Outline each blood parasite and name the species.
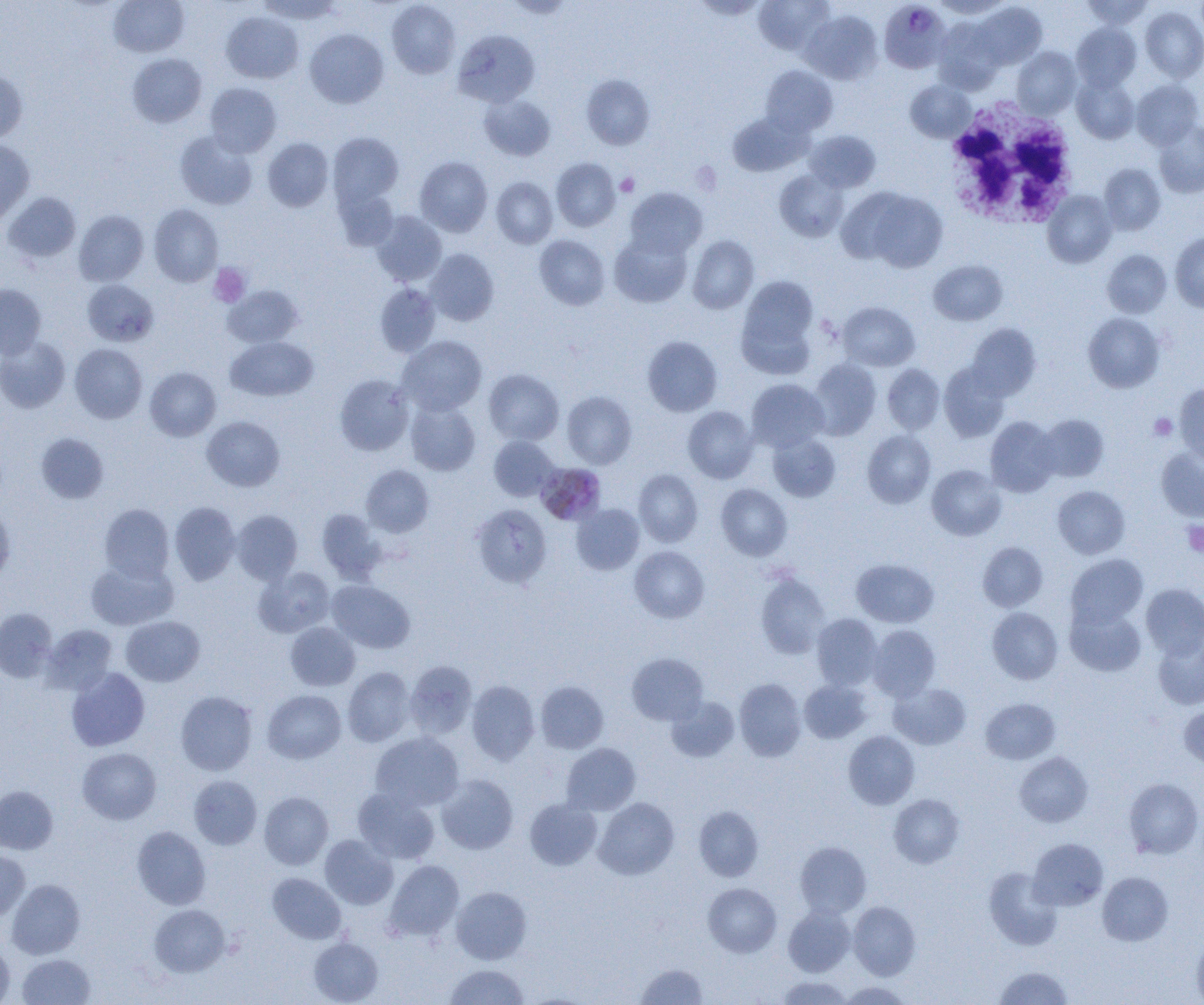

Approximate bounding boxes as named x1/y1/x2/y2 corners in pixels.
Plasmodium malariae-infected red blood cells: (x1=879, y1=1, x2=952, y2=74), (x1=538, y1=463, x2=608, y2=522).
No Plasmodium falciparum, Plasmodium ovale, Plasmodium vivax, Babesia divergens, or Trypanosoma brucei observed.

Platelet locations: (x1=616, y1=173, x2=639, y2=196), (x1=209, y1=263, x2=250, y2=307), (x1=1149, y1=414, x2=1177, y2=440), (x1=1182, y1=521, x2=1204, y2=557). White blood cell locations: (x1=941, y1=98, x2=1082, y2=229). Uninfected red blood cell locations: (x1=109, y1=0, x2=189, y2=57), (x1=257, y1=0, x2=344, y2=24), (x1=753, y1=0, x2=833, y2=55), (x1=930, y1=0, x2=1011, y2=19), (x1=1081, y1=0, x2=1154, y2=30), (x1=386, y1=1, x2=460, y2=78), (x1=972, y1=3, x2=1047, y2=69), (x1=1140, y1=5, x2=1204, y2=83), (x1=801, y1=10, x2=883, y2=85), (x1=221, y1=12, x2=303, y2=84), (x1=933, y1=19, x2=1005, y2=93), (x1=1071, y1=23, x2=1141, y2=92), (x1=305, y1=29, x2=389, y2=108), (x1=454, y1=29, x2=539, y2=107), (x1=1012, y1=47, x2=1081, y2=119), (x1=128, y1=53, x2=207, y2=127), (x1=760, y1=65, x2=837, y2=137), (x1=0, y1=68, x2=28, y2=143), (x1=581, y1=74, x2=655, y2=150), (x1=1072, y1=75, x2=1139, y2=144), (x1=1131, y1=79, x2=1203, y2=149), (x1=905, y1=80, x2=975, y2=142), (x1=205, y1=83, x2=281, y2=157), (x1=479, y1=93, x2=555, y2=161), (x1=728, y1=112, x2=810, y2=176), (x1=1154, y1=121, x2=1204, y2=198), (x1=804, y1=130, x2=880, y2=192), (x1=175, y1=131, x2=258, y2=209), (x1=328, y1=133, x2=403, y2=208), (x1=263, y1=137, x2=333, y2=212), (x1=0, y1=140, x2=34, y2=225), (x1=415, y1=156, x2=492, y2=237), (x1=551, y1=158, x2=620, y2=231), (x1=1099, y1=164, x2=1165, y2=235), (x1=774, y1=170, x2=848, y2=242), (x1=491, y1=177, x2=557, y2=248), (x1=334, y1=187, x2=399, y2=251), (x1=624, y1=187, x2=707, y2=258), (x1=851, y1=189, x2=948, y2=272), (x1=1043, y1=191, x2=1117, y2=268), (x1=3, y1=192, x2=81, y2=263), (x1=149, y1=204, x2=223, y2=286), (x1=74, y1=210, x2=149, y2=286), (x1=371, y1=211, x2=447, y2=287), (x1=609, y1=232, x2=692, y2=308), (x1=1170, y1=232, x2=1204, y2=313), (x1=534, y1=235, x2=610, y2=310), (x1=687, y1=235, x2=759, y2=314), (x1=425, y1=249, x2=499, y2=325), (x1=1102, y1=249, x2=1172, y2=318), (x1=928, y1=260, x2=1007, y2=325), (x1=738, y1=275, x2=819, y2=366), (x1=82, y1=279, x2=158, y2=347), (x1=375, y1=283, x2=440, y2=357), (x1=0, y1=284, x2=46, y2=359), (x1=223, y1=285, x2=303, y2=348), (x1=838, y1=302, x2=920, y2=371), (x1=1083, y1=312, x2=1165, y2=392), (x1=966, y1=323, x2=1041, y2=401), (x1=225, y1=336, x2=318, y2=401), (x1=397, y1=336, x2=487, y2=415), (x1=642, y1=336, x2=723, y2=416), (x1=0, y1=337, x2=70, y2=413), (x1=70, y1=344, x2=147, y2=423), (x1=808, y1=358, x2=882, y2=440), (x1=882, y1=363, x2=945, y2=434), (x1=939, y1=363, x2=1010, y2=442), (x1=145, y1=367, x2=221, y2=441), (x1=484, y1=368, x2=564, y2=445), (x1=334, y1=374, x2=414, y2=456), (x1=746, y1=379, x2=829, y2=452), (x1=1174, y1=383, x2=1204, y2=466), (x1=561, y1=391, x2=636, y2=469), (x1=406, y1=400, x2=481, y2=476), (x1=682, y1=406, x2=758, y2=483), (x1=1037, y1=414, x2=1109, y2=482), (x1=202, y1=416, x2=284, y2=491), (x1=985, y1=416, x2=1060, y2=497), (x1=862, y1=430, x2=936, y2=508), (x1=36, y1=433, x2=109, y2=504), (x1=768, y1=434, x2=840, y2=502), (x1=489, y1=435, x2=559, y2=501), (x1=1156, y1=448, x2=1204, y2=521), (x1=927, y1=464, x2=1006, y2=540), (x1=361, y1=465, x2=434, y2=537), (x1=634, y1=469, x2=703, y2=546), (x1=716, y1=484, x2=792, y2=560), (x1=1052, y1=485, x2=1130, y2=559), (x1=169, y1=502, x2=241, y2=585), (x1=100, y1=503, x2=175, y2=581), (x1=472, y1=503, x2=552, y2=588), (x1=572, y1=504, x2=644, y2=574), (x1=0, y1=505, x2=15, y2=583), (x1=316, y1=509, x2=386, y2=582), (x1=232, y1=510, x2=303, y2=584), (x1=978, y1=542, x2=1048, y2=611), (x1=629, y1=546, x2=709, y2=623), (x1=1065, y1=554, x2=1148, y2=630), (x1=851, y1=558, x2=938, y2=627), (x1=86, y1=559, x2=178, y2=630), (x1=254, y1=567, x2=335, y2=637), (x1=755, y1=571, x2=830, y2=659), (x1=327, y1=580, x2=415, y2=653), (x1=1141, y1=583, x2=1204, y2=659), (x1=1065, y1=605, x2=1146, y2=676), (x1=987, y1=607, x2=1063, y2=684), (x1=0, y1=608, x2=57, y2=683), (x1=811, y1=613, x2=882, y2=690), (x1=121, y1=616, x2=205, y2=686), (x1=285, y1=622, x2=360, y2=690), (x1=42, y1=624, x2=117, y2=694), (x1=867, y1=624, x2=940, y2=701), (x1=1153, y1=634, x2=1204, y2=709), (x1=627, y1=652, x2=708, y2=725), (x1=405, y1=660, x2=477, y2=738), (x1=66, y1=667, x2=150, y2=751), (x1=342, y1=667, x2=415, y2=746), (x1=734, y1=678, x2=806, y2=761), (x1=466, y1=680, x2=539, y2=764), (x1=536, y1=680, x2=608, y2=753), (x1=799, y1=680, x2=871, y2=743), (x1=889, y1=683, x2=971, y2=749), (x1=175, y1=690, x2=257, y2=775), (x1=263, y1=690, x2=345, y2=763), (x1=666, y1=696, x2=740, y2=763), (x1=981, y1=698, x2=1060, y2=764), (x1=1178, y1=706, x2=1204, y2=769), (x1=843, y1=730, x2=920, y2=809), (x1=371, y1=732, x2=463, y2=811), (x1=562, y1=743, x2=640, y2=814), (x1=78, y1=747, x2=161, y2=824), (x1=1015, y1=752, x2=1092, y2=827), (x1=436, y1=774, x2=518, y2=853), (x1=189, y1=775, x2=262, y2=849), (x1=1124, y1=778, x2=1203, y2=859), (x1=0, y1=786, x2=57, y2=854), (x1=353, y1=788, x2=440, y2=864), (x1=259, y1=792, x2=333, y2=869), (x1=889, y1=794, x2=965, y2=868), (x1=594, y1=797, x2=679, y2=880), (x1=525, y1=798, x2=602, y2=870), (x1=694, y1=805, x2=763, y2=881), (x1=132, y1=826, x2=211, y2=910), (x1=319, y1=835, x2=398, y2=909), (x1=1028, y1=838, x2=1108, y2=911), (x1=795, y1=841, x2=871, y2=918), (x1=0, y1=848, x2=30, y2=919), (x1=384, y1=860, x2=463, y2=941), (x1=984, y1=867, x2=1062, y2=950), (x1=267, y1=872, x2=346, y2=944), (x1=1097, y1=872, x2=1173, y2=945), (x1=7, y1=879, x2=85, y2=959), (x1=703, y1=883, x2=781, y2=957), (x1=451, y1=887, x2=532, y2=964), (x1=848, y1=901, x2=921, y2=980), (x1=149, y1=904, x2=230, y2=976), (x1=783, y1=906, x2=855, y2=976), (x1=1191, y1=933, x2=1204, y2=1004), (x1=309, y1=937, x2=383, y2=1005), (x1=0, y1=939, x2=15, y2=1004), (x1=17, y1=954, x2=95, y2=1005), (x1=635, y1=963, x2=708, y2=1005), (x1=444, y1=964, x2=529, y2=1004), (x1=993, y1=965, x2=1073, y2=1004), (x1=776, y1=976, x2=853, y2=1004), (x1=839, y1=981, x2=913, y2=1004). Slide-level diagnosis: Plasmodium malariae. Single field of view. Image is 1204×1005 pixels. 1000x magnification. Optical microscopy. Thin blood film.